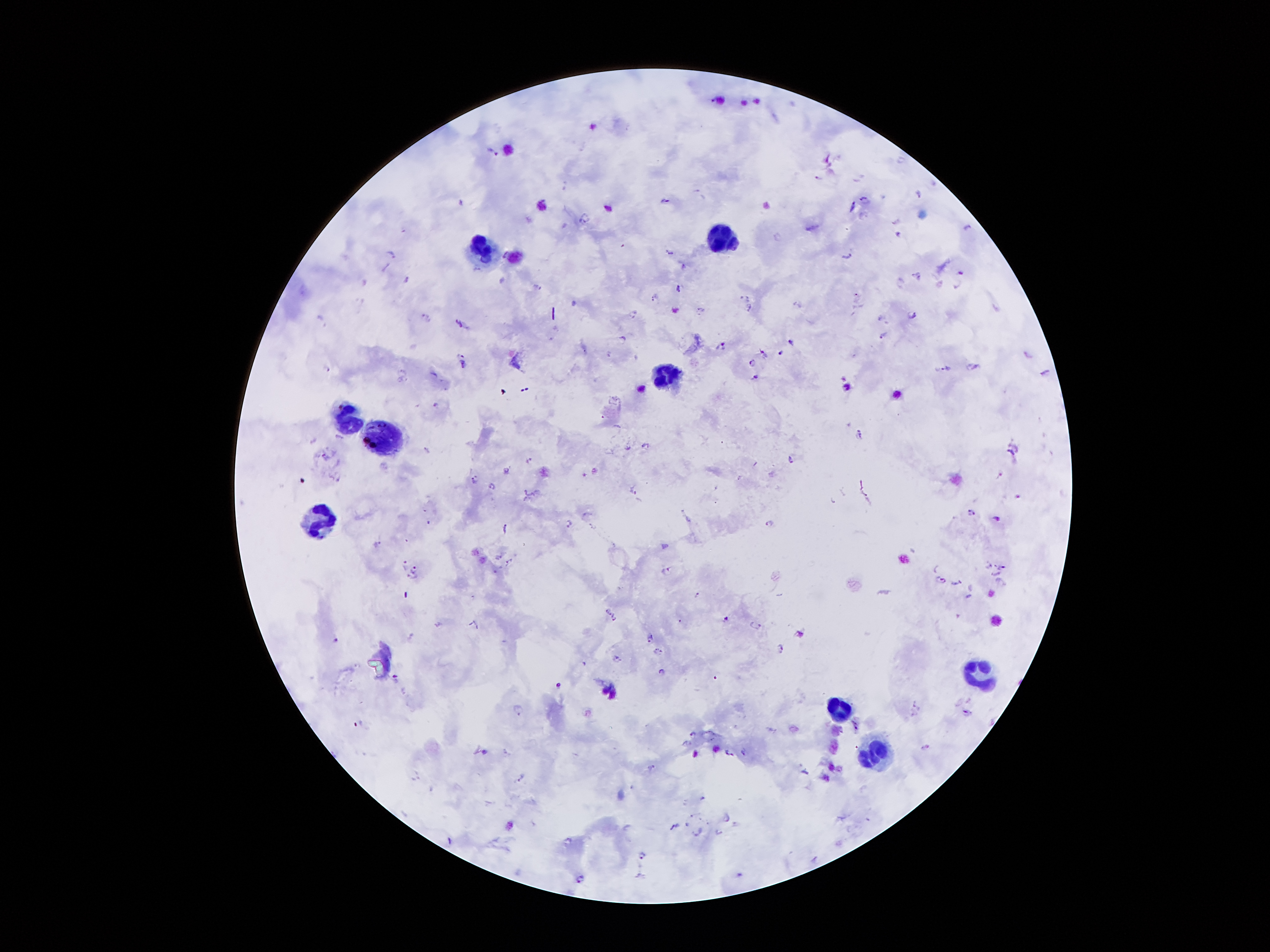

Approximate centers as {x, y} in pixels. Leukocyte locations: {726, 239}, {481, 250}, {664, 374}, {348, 419}, {383, 438}, {317, 518}, {979, 677}, {841, 709}, {877, 753}. Malaria parasite locations: {492, 151}, {817, 177}, {919, 193}, {865, 200}, {664, 201}, {851, 207}, {897, 220}, {966, 227}, {897, 234}, {776, 237}, {503, 252}, {670, 253}, {846, 254}, {390, 256}, {683, 264}, {960, 272}, {914, 274}, {406, 278}, {901, 281}, {938, 283}, {536, 284}, {956, 287}, {678, 288}, {654, 298}, {747, 298}, {748, 308}, {701, 309}, {632, 314}, {912, 314}, {425, 318}, {882, 320}, {461, 324}, {882, 335}, {623, 339}, {791, 342}, {721, 345}, {763, 353}, {780, 353}, {1026, 355}, {461, 362}, {751, 362}, {973, 367}, {946, 368}, {1045, 371}, {754, 376}, {842, 378}, {435, 406}, {647, 445}, {325, 456}, {528, 460}, {791, 460}, {998, 474}, {472, 478}, {491, 486}, {632, 490}, {970, 512}, {997, 519}, {568, 523}, {769, 523}, {504, 528}, {378, 545}, {498, 557}, {509, 561}, {404, 562}, {989, 567}, {1001, 567}, {416, 569}, {666, 569}, {995, 575}, {409, 578}, {941, 579}, {957, 583}, {696, 594}, {609, 612}, {725, 617}, {614, 619}, {438, 624}, {756, 625}, {650, 638}, {335, 639}, {780, 647}, {658, 651}, {617, 659}, {660, 672}, {395, 676}, {558, 685}, {519, 709}, {968, 713}, {693, 735}, {926, 746}, {485, 751}, {729, 751}, {650, 767}, {806, 772}, {520, 777}, {726, 817}, {717, 830}, {696, 831}, {641, 853}, {580, 877}. Image is 1270×952 pixels. Photographed through the microscope eyepiece with a smartphone camera. Giemsa-stained preparation. Single field of view. Thick blood film. 100x magnification. Patient malaria status: infected with Plasmodium falciparum.